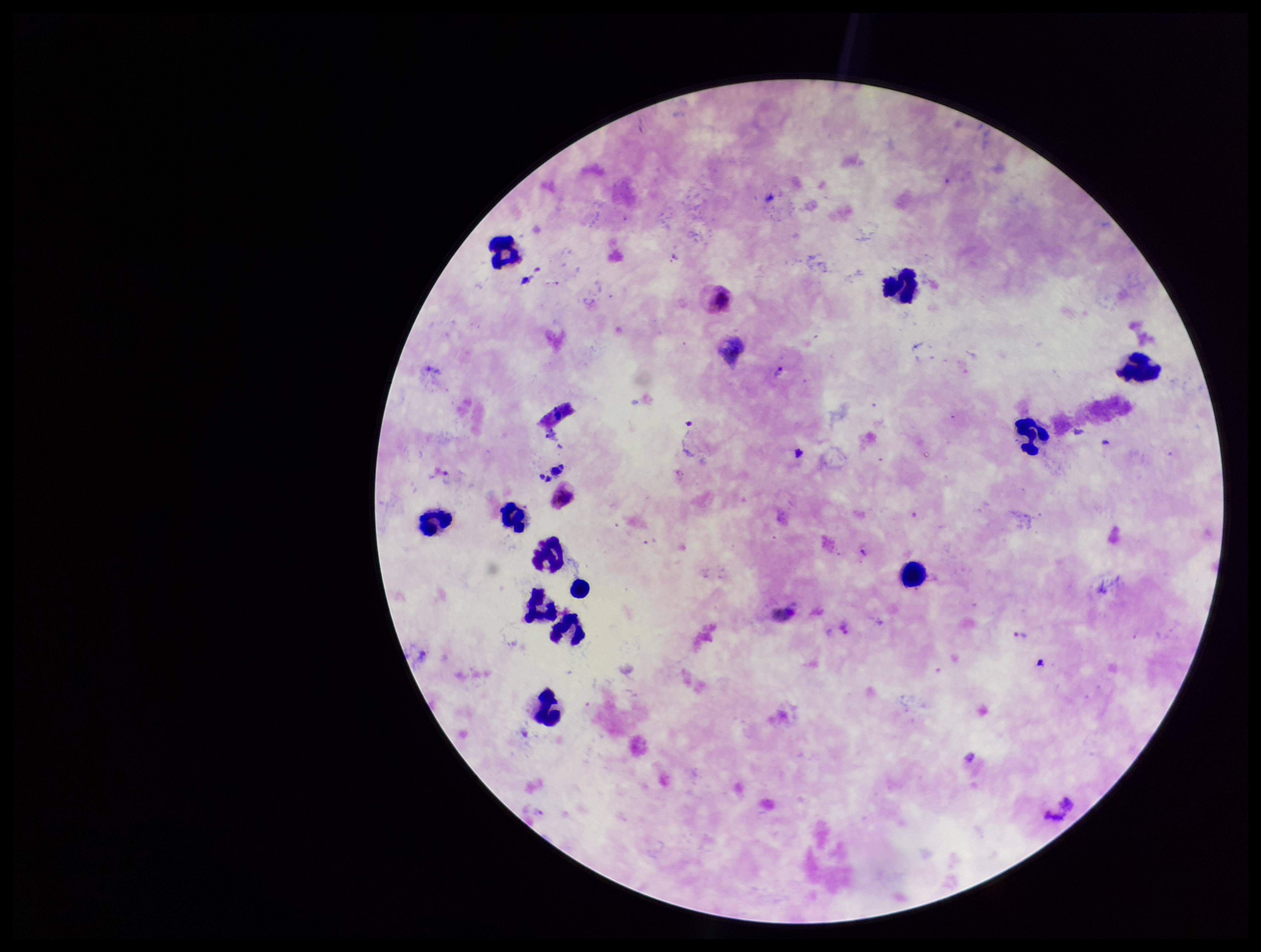

Summary:
  - Parasite count: 1
  - Species reported for this patient: Plasmodium vivax
  - Image size: 1261×952 pixels
  - Preparation: thick
  - Leukocyte count: 12
  - Plasmodium parasites: seen
  - Stain: Giemsa
  - Field of view: one from this slide
  - Patient malaria status: infected
  - Capture: smartphone photograph through the microscope eyepiece